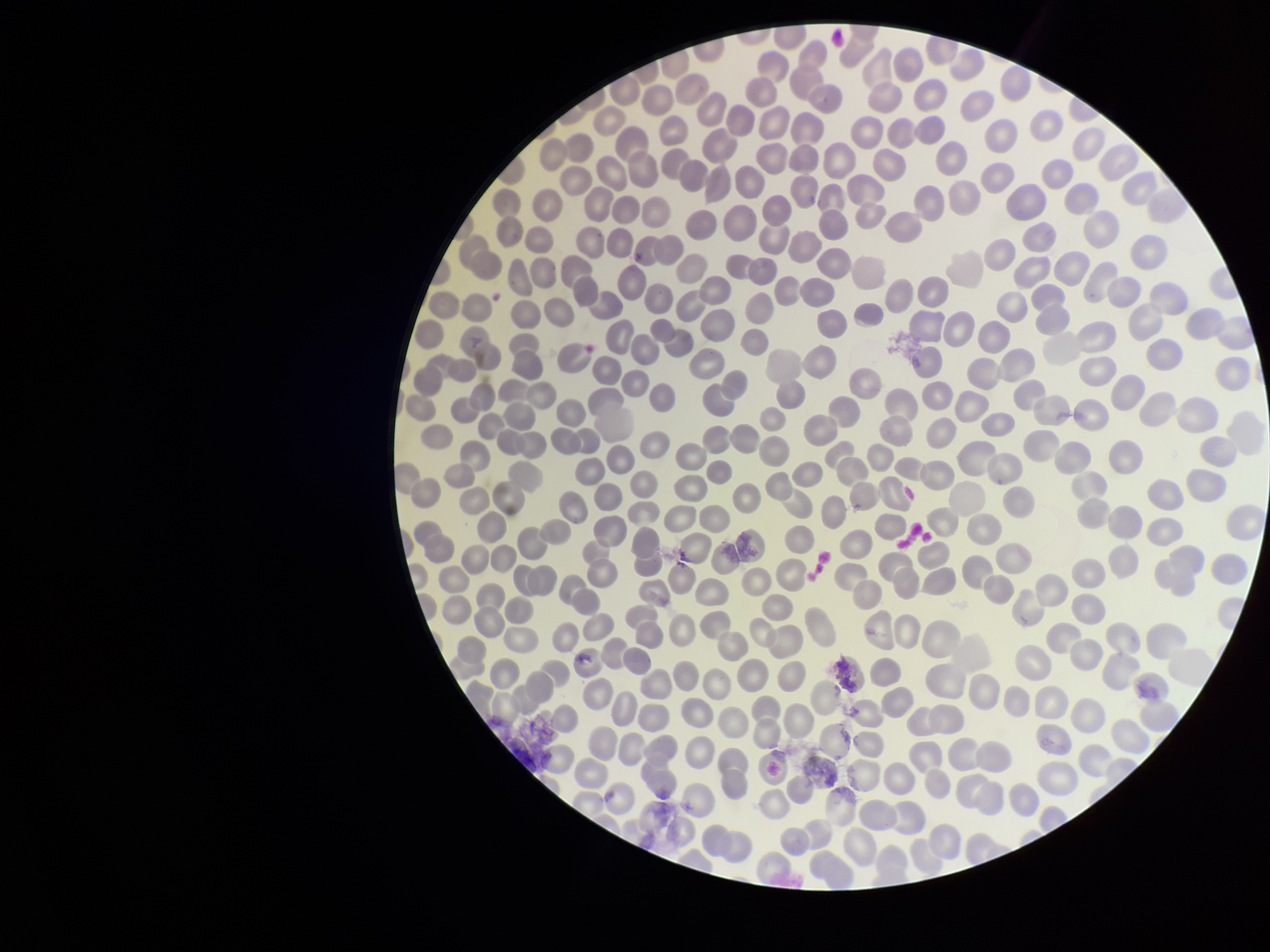
Stained with Giemsa. Parasitized red blood cells: none detected. Red blood cell count: 311. Smartphone photograph taken through the eyepiece of a microscope. One field from this slide. Patient malaria status: negative. Parasitized red blood cell count: 0. Preparation: thin blood smear. Image is 1270×952 pixels.